Assess this cell for malaria.
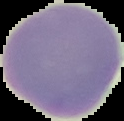

It is uninfected.

Summary:
  - Image type: cell region segmented out of the field of view; surrounding area masked to black
  - Preparation: thin blood film
  - Image size: 124×121 pixels